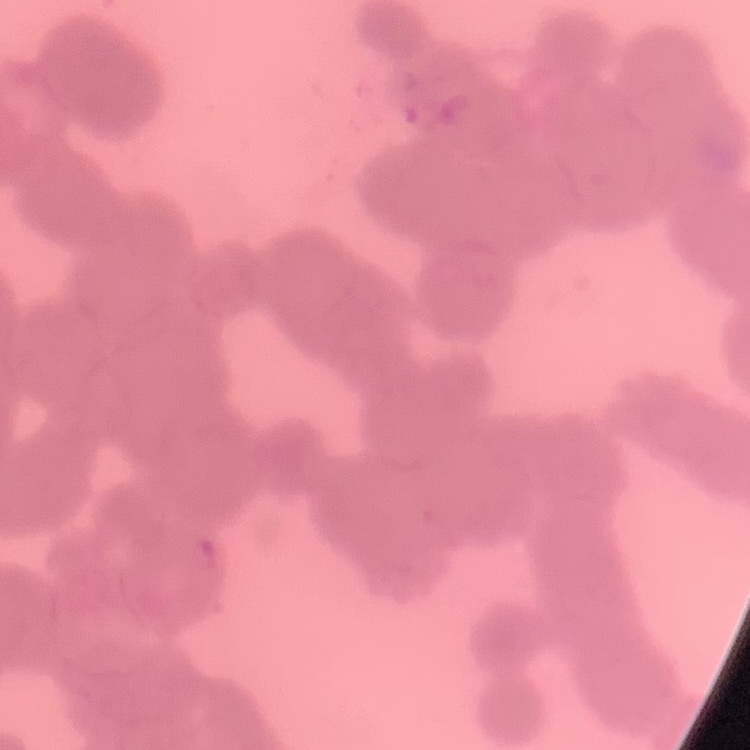
erythrocyte morphology = rouleaux formation
stain = Field's or Giemsa
preparation = thin blood film
image type = one tile cut from a larger photomicrograph